Name the parasite shown.
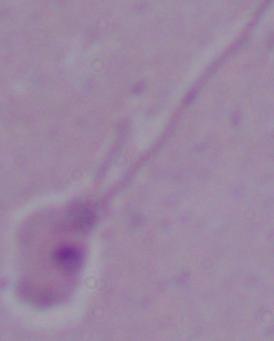

This is Leishmania.

magnification = 1000x
modality = micrograph